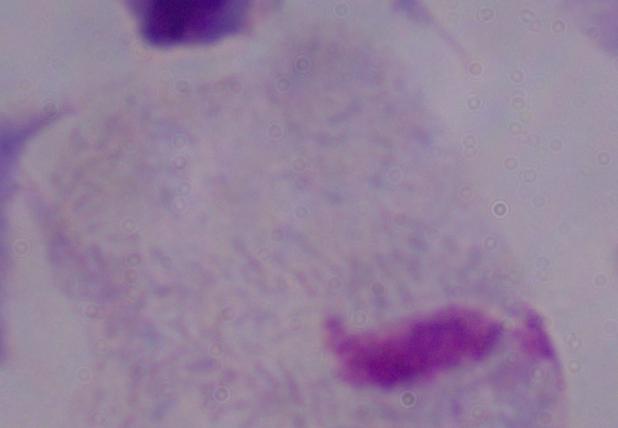
Captured at 1000x magnification. Photomicrograph. A trichomonad is seen.